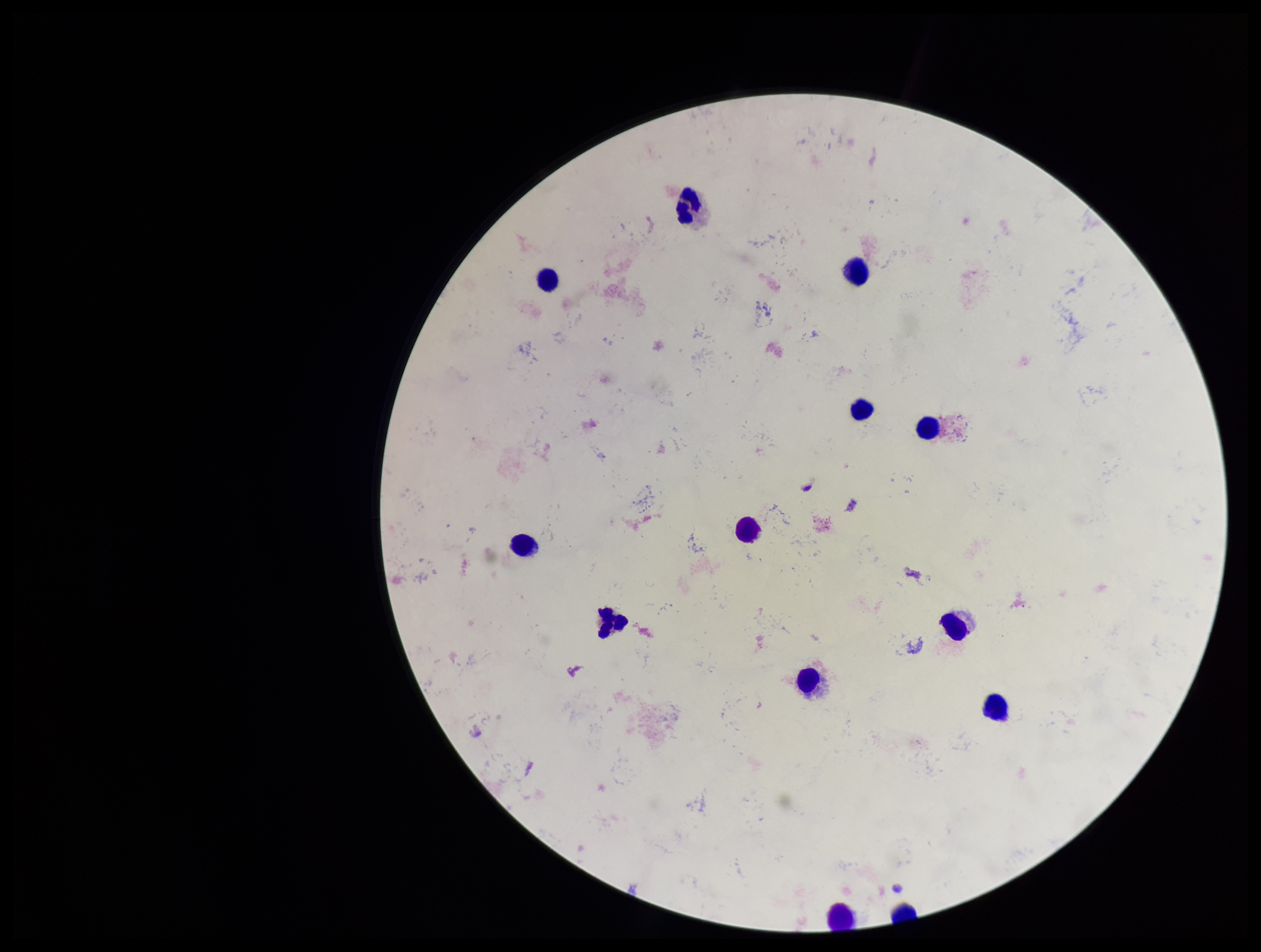
Summary:
  - Field of view: single
  - Image size: 1261×952 pixels
  - Patient malaria status: negative
  - Plasmodium parasites: none identified
  - Preparation: thick blood smear
  - Stain: Giemsa
  - Leukocyte count: 13
  - Capture: smartphone photograph through the microscope eyepiece
  - Parasite count: 0